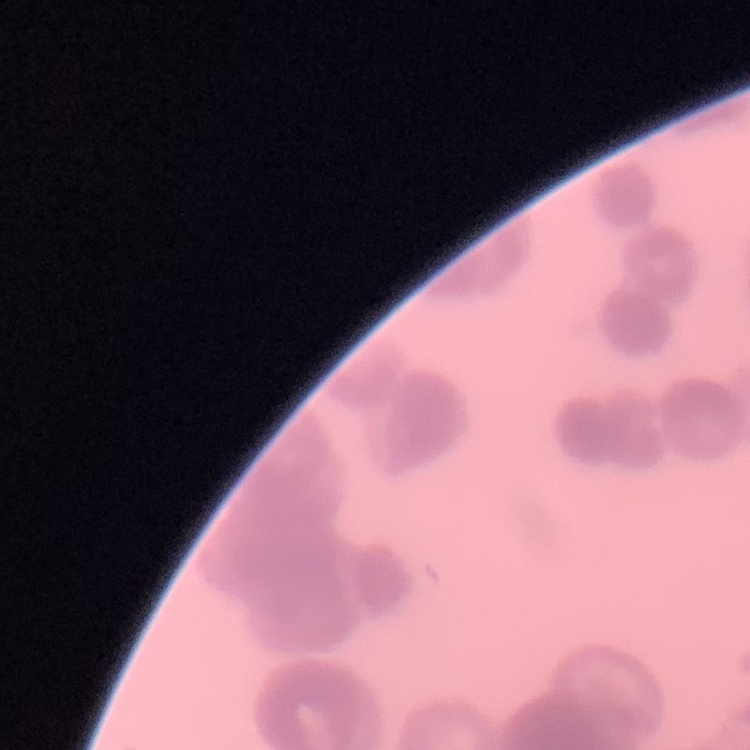

The red blood cells show rouleaux formation. Stained with either Field's or Giemsa. Thin peripheral smear. Square crop of a larger photomicrograph.